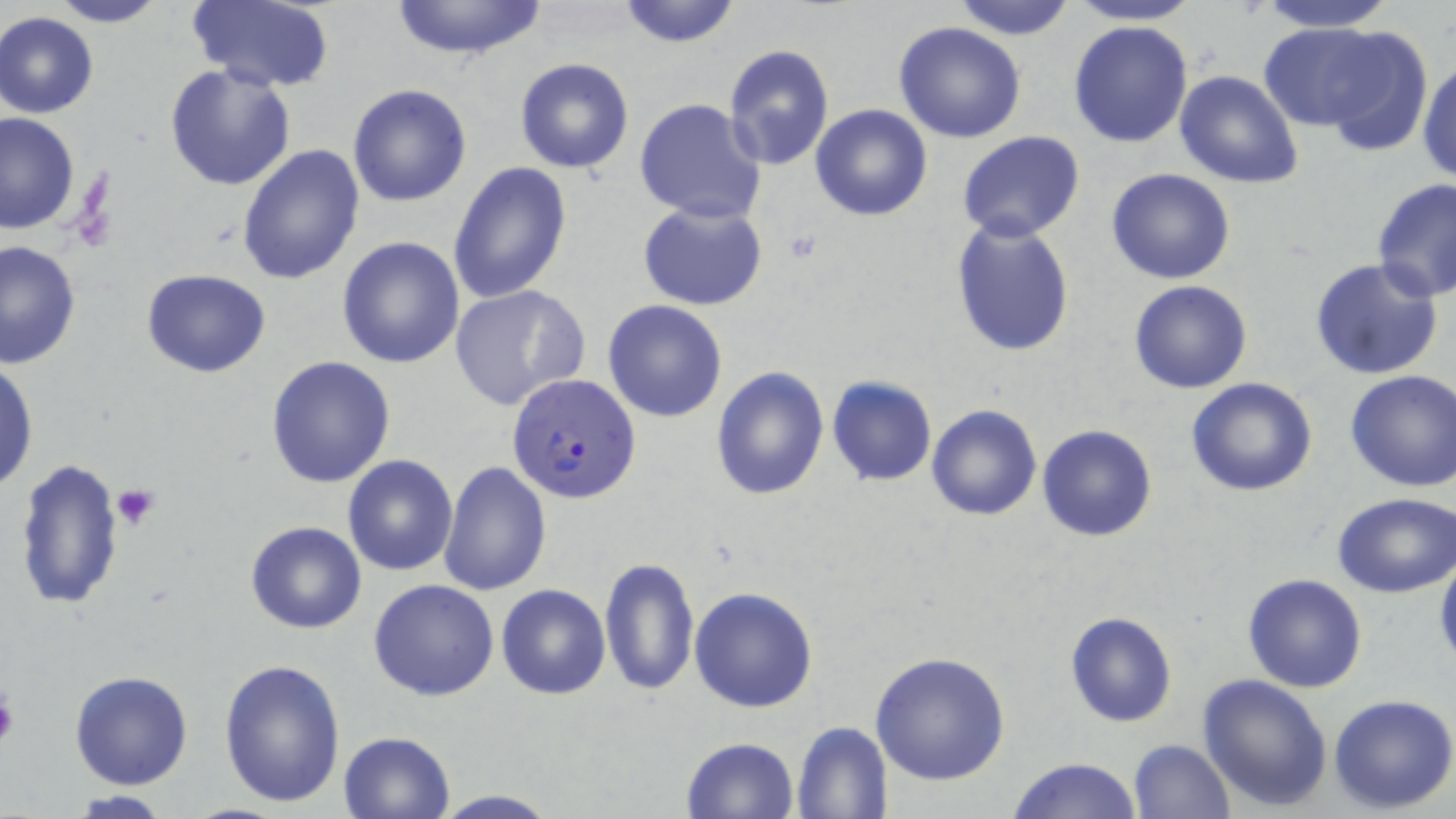 Approximate bounding boxes as (x1, y1, x2, y2) in pixels. Plasmodium falciparum-infected red blood cell locations: (506, 374, 640, 503). Uninfected red blood cell locations: (44, 0, 169, 27), (186, 0, 337, 91), (386, 0, 547, 60), (951, 0, 1077, 39), (1060, 0, 1208, 25), (1252, 0, 1399, 31), (614, 1, 743, 48), (1, 11, 99, 118), (1067, 20, 1194, 148), (893, 21, 1027, 143), (1261, 22, 1395, 130), (1314, 27, 1434, 157), (722, 44, 834, 172), (1417, 57, 1456, 186), (515, 58, 634, 173), (165, 63, 296, 192), (1175, 71, 1303, 189), (347, 84, 472, 207), (634, 98, 766, 224), (809, 104, 933, 221), (0, 112, 81, 236), (957, 131, 1085, 242), (237, 144, 366, 287), (447, 162, 573, 306), (1105, 166, 1237, 285), (1371, 177, 1456, 301), (638, 201, 769, 310), (950, 220, 1075, 357), (336, 236, 466, 369), (0, 239, 81, 371), (1308, 257, 1444, 382), (140, 269, 271, 378), (1127, 279, 1254, 394), (449, 284, 590, 411), (602, 300, 728, 421), (266, 355, 397, 488), (1, 360, 37, 493), (710, 366, 830, 500), (1344, 369, 1456, 493), (826, 377, 937, 486), (1185, 377, 1318, 497), (925, 403, 1042, 521), (1036, 423, 1158, 541), (341, 454, 458, 576), (13, 458, 125, 612), (438, 459, 553, 596), (1333, 492, 1455, 597), (245, 521, 366, 635), (1434, 555, 1456, 669), (599, 557, 699, 697), (1241, 572, 1368, 694), (368, 579, 500, 701), (496, 584, 610, 699), (689, 587, 819, 712), (1065, 611, 1178, 728), (869, 650, 1010, 786), (217, 656, 346, 808), (69, 670, 195, 789), (1197, 673, 1333, 812), (1328, 693, 1456, 812), (790, 720, 893, 818), (337, 732, 456, 819), (681, 736, 799, 819), (1128, 738, 1235, 819), (1008, 756, 1142, 819), (426, 789, 563, 819), (65, 792, 175, 818). Platelet locations: (115, 485, 162, 531), (0, 685, 18, 753). Slide-level diagnosis: Plasmodium falciparum. May-Grünwald-Giemsa stain. Thin blood film. 1000x magnification. Image is 1456×819 pixels. Single field of view. Light microscopy.